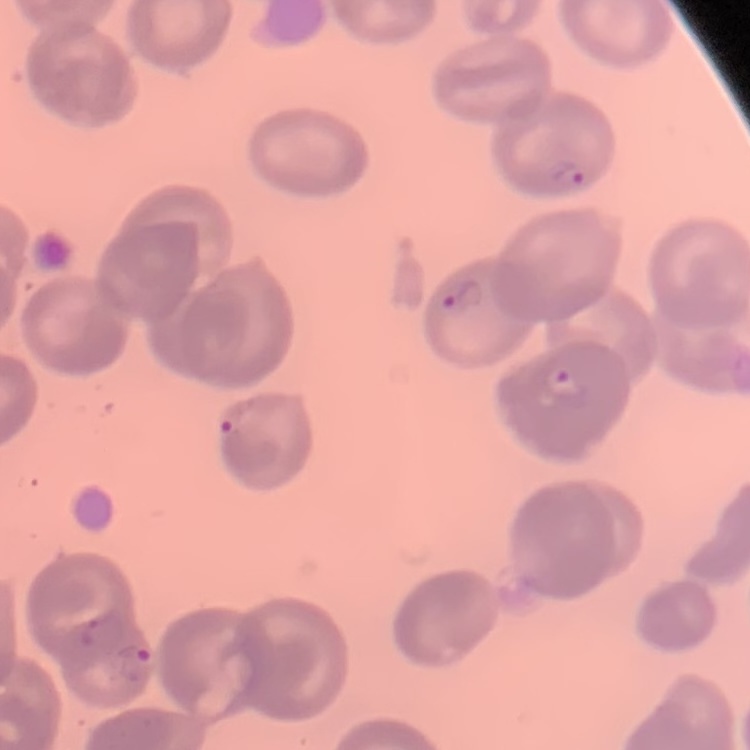

Summary:
  - Erythrocyte morphology: no rouleaux formation
  - Preparation: thin peripheral smear
  - Stain: Field's or Giemsa
  - Image type: square crop of a larger photomicrograph